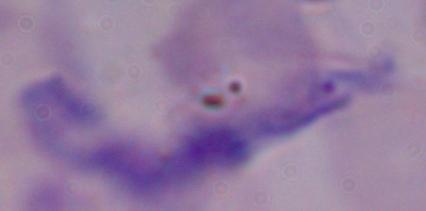
Summary:
  - Identification: trypanosome
  - Magnification: 1000x
  - Modality: micrograph